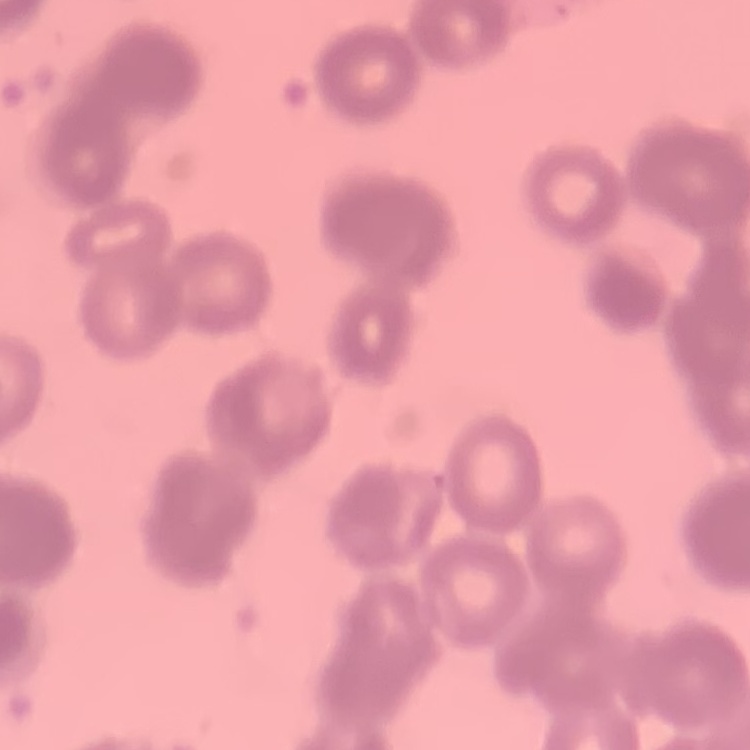
The red blood cells exhibit rouleaux formation. Thin blood film. Square crop of a larger photomicrograph. Field's or Giemsa stain.